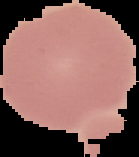 Image is 139×157 pixels. From a thin blood film. Result: negative for Plasmodium parasites. Segmented cell region on a black background.